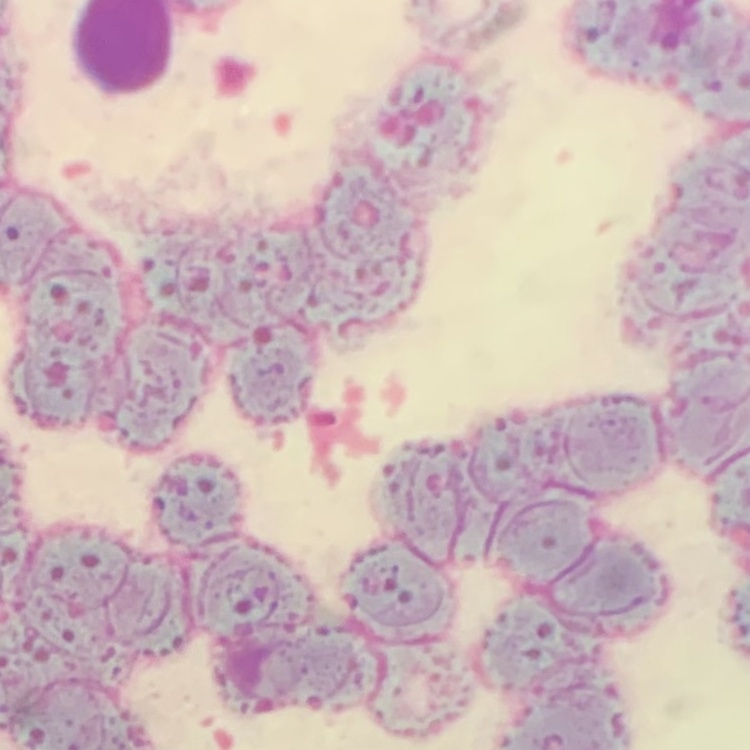

Summary:
  - Red blood cell morphology: rouleaux formation
  - Image type: one tile cut from a larger photomicrograph
  - Preparation: thin peripheral smear
  - Stain: Field's or Giemsa